Classify this cell by malaria status.
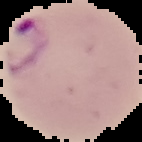

It is parasitized.

Cell region segmented out of the field of view; the surrounding area is masked to black. Image is 142×142 pixels. From a thin blood film.